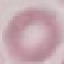
Summary:
  - Malaria status: uninfected
  - Capture: smartphone through the microscope eyepiece
  - Preparation: thin blood smear
  - Image type: automatically extracted cell patch, resized to 64 × 64 pixels
  - Stain: Giemsa